Identify the blood parasite species.
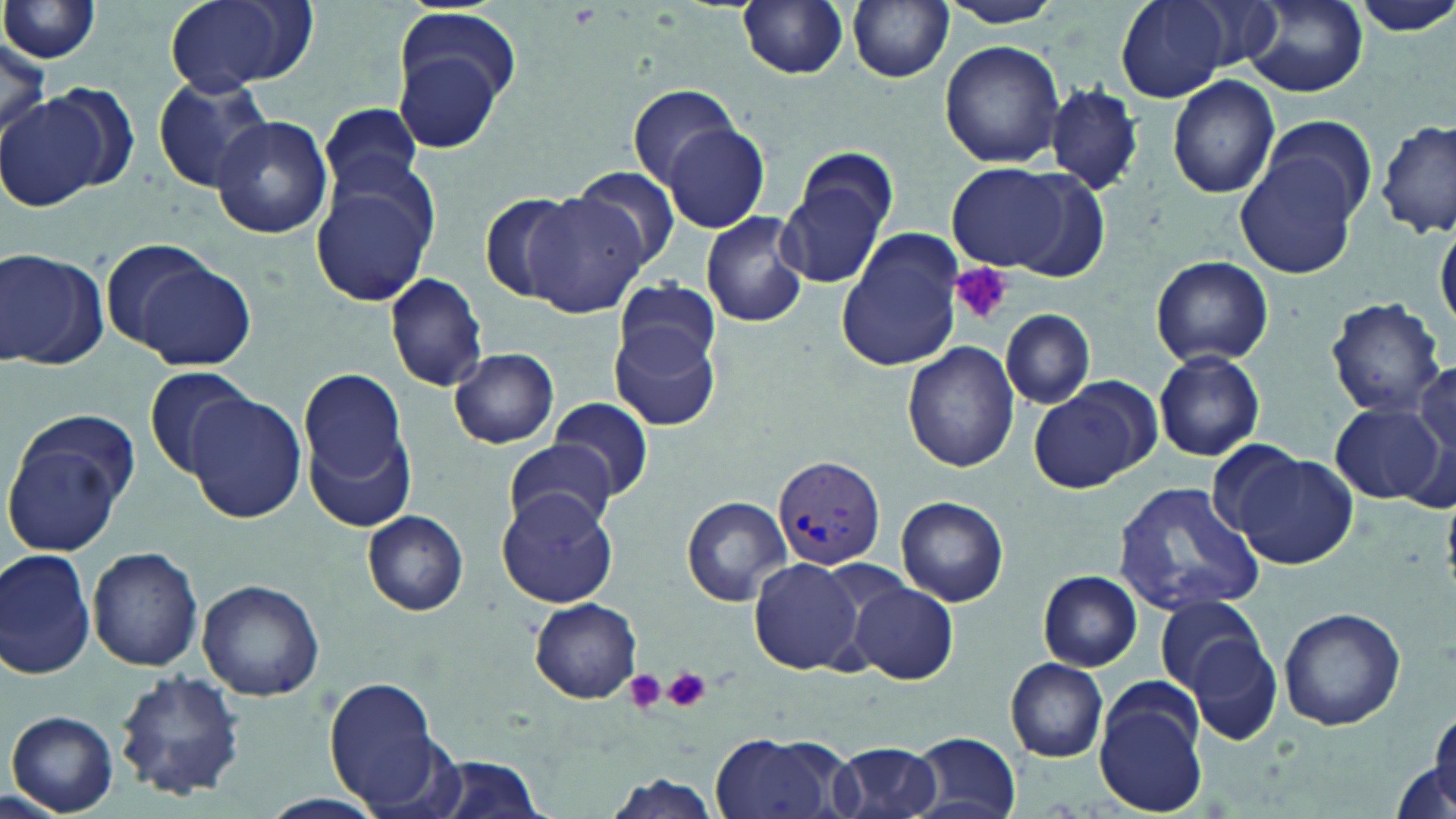

Plasmodium vivax.

Summary:
  - Coordinate format: approximate bounding boxes as named x1/y1/x2/y2 corners in pixels
  - Plasmodium vivax-infected red blood cell locations: (x1=772, y1=453, x2=886, y2=572)
  - Platelet locations: (x1=951, y1=262, x2=1012, y2=325), (x1=663, y1=665, x2=711, y2=712), (x1=623, y1=668, x2=666, y2=713)
  - Uninfected red blood cell locations: (x1=0, y1=0, x2=103, y2=65), (x1=164, y1=0, x2=315, y2=93), (x1=937, y1=0, x2=1068, y2=29), (x1=1117, y1=0, x2=1229, y2=103), (x1=1178, y1=0, x2=1284, y2=72), (x1=737, y1=1, x2=850, y2=79), (x1=847, y1=1, x2=954, y2=83), (x1=1350, y1=1, x2=1456, y2=38), (x1=1241, y1=3, x2=1367, y2=95), (x1=389, y1=28, x2=513, y2=155), (x1=0, y1=31, x2=50, y2=139), (x1=940, y1=40, x2=1065, y2=170), (x1=152, y1=74, x2=275, y2=193), (x1=1168, y1=75, x2=1281, y2=198), (x1=628, y1=83, x2=744, y2=189), (x1=1046, y1=84, x2=1141, y2=194), (x1=2, y1=93, x2=106, y2=213), (x1=319, y1=102, x2=424, y2=199), (x1=1255, y1=111, x2=1381, y2=226), (x1=210, y1=116, x2=334, y2=241), (x1=1378, y1=119, x2=1455, y2=240), (x1=662, y1=123, x2=771, y2=233), (x1=1237, y1=152, x2=1364, y2=278), (x1=779, y1=157, x2=894, y2=289), (x1=946, y1=162, x2=1070, y2=272), (x1=570, y1=165, x2=681, y2=272), (x1=309, y1=172, x2=437, y2=305), (x1=523, y1=190, x2=652, y2=318), (x1=480, y1=191, x2=589, y2=304), (x1=701, y1=210, x2=809, y2=328), (x1=1435, y1=222, x2=1455, y2=332), (x1=835, y1=230, x2=964, y2=373), (x1=98, y1=238, x2=222, y2=354), (x1=0, y1=248, x2=106, y2=370), (x1=1149, y1=254, x2=1274, y2=367), (x1=129, y1=257, x2=257, y2=372), (x1=384, y1=272, x2=489, y2=393), (x1=614, y1=277, x2=720, y2=372), (x1=1325, y1=296, x2=1446, y2=419), (x1=1000, y1=309, x2=1094, y2=411), (x1=608, y1=322, x2=721, y2=432), (x1=902, y1=341, x2=1021, y2=472), (x1=448, y1=348, x2=558, y2=449), (x1=1152, y1=350, x2=1266, y2=461), (x1=1412, y1=364, x2=1455, y2=466), (x1=141, y1=365, x2=259, y2=479), (x1=299, y1=370, x2=409, y2=491), (x1=1031, y1=382, x2=1153, y2=495), (x1=186, y1=390, x2=307, y2=523), (x1=548, y1=398, x2=655, y2=502), (x1=1328, y1=401, x2=1445, y2=505), (x1=304, y1=420, x2=415, y2=531), (x1=3, y1=428, x2=132, y2=557), (x1=499, y1=442, x2=617, y2=530), (x1=1233, y1=452, x2=1358, y2=567), (x1=1113, y1=480, x2=1263, y2=616), (x1=498, y1=486, x2=619, y2=613), (x1=681, y1=495, x2=792, y2=605), (x1=895, y1=496, x2=1009, y2=607), (x1=360, y1=508, x2=470, y2=616), (x1=88, y1=544, x2=205, y2=671), (x1=1, y1=547, x2=97, y2=680), (x1=750, y1=557, x2=865, y2=675), (x1=1038, y1=570, x2=1140, y2=671), (x1=850, y1=579, x2=959, y2=684), (x1=197, y1=580, x2=325, y2=700), (x1=1156, y1=594, x2=1267, y2=696), (x1=530, y1=598, x2=642, y2=704), (x1=1279, y1=605, x2=1406, y2=731), (x1=1187, y1=636, x2=1283, y2=744), (x1=1003, y1=657, x2=1109, y2=762), (x1=115, y1=670, x2=246, y2=800), (x1=325, y1=676, x2=445, y2=811), (x1=1094, y1=685, x2=1207, y2=814), (x1=7, y1=711, x2=120, y2=815), (x1=1422, y1=711, x2=1456, y2=817), (x1=708, y1=730, x2=847, y2=819), (x1=911, y1=733, x2=1021, y2=818), (x1=828, y1=740, x2=944, y2=819), (x1=424, y1=755, x2=549, y2=819), (x1=1392, y1=758, x2=1453, y2=818), (x1=604, y1=773, x2=723, y2=818), (x1=259, y1=791, x2=389, y2=819)
  - Modality: optical microscopy
  - Stain: May-Grünwald-Giemsa
  - Image size: 1456×819 pixels
  - Field of view: one of a larger specimen
  - Magnification: 1000x
  - Preparation: thin blood film